Locate and identify every blood parasite.
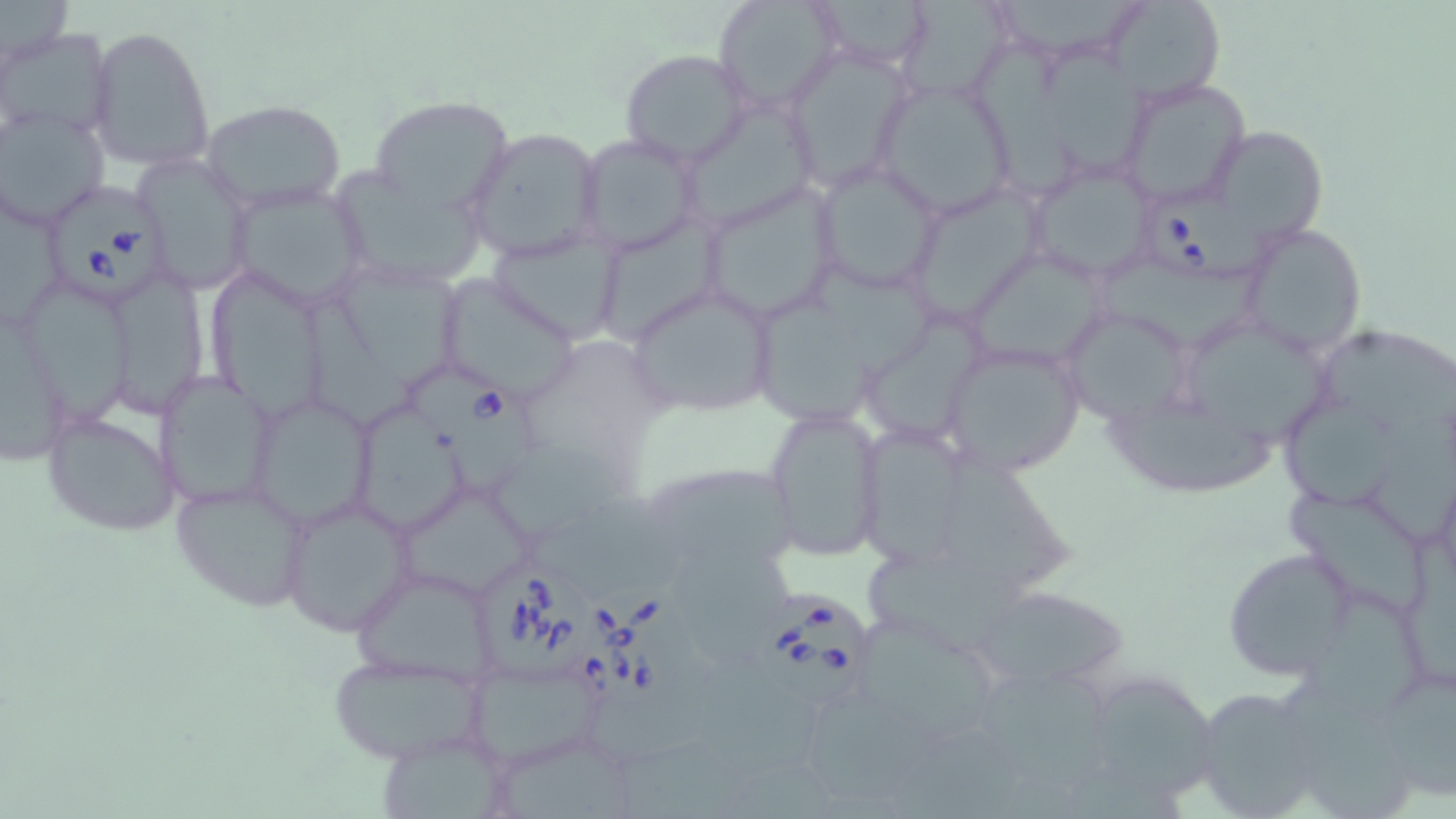

Approximate bounding boxes as (x1,y1)-(x2,y2) corner pairs in pixels.
Babesia divergens-infected red blood cells: (49,186)-(164,306), (1144,189)-(1271,283), (405,367)-(540,498), (477,565)-(592,681), (576,577)-(698,712), (750,590)-(873,713).
No Plasmodium falciparum, Plasmodium ovale, Plasmodium malariae, Plasmodium vivax, or Trypanosoma brucei observed.

slide-level diagnosis = Babesia divergens
preparation = thin blood smear
field of view = one of a larger specimen
magnification = 1000x
stain = May-Grünwald-Giemsa
modality = light microscopy
uninfected red blood cell locations = approximate bounding boxes as (x1,y1)-(x2,y2) corner pairs in pixels: (0,0)-(72,63), (714,0)-(841,115), (803,0)-(935,72), (998,0)-(1151,53), (1109,0)-(1223,105), (896,1)-(1016,104), (86,24)-(216,172), (0,29)-(118,146), (978,33)-(1081,195), (780,44)-(916,193), (1048,49)-(1156,180), (619,50)-(752,166), (1116,76)-(1252,210), (877,80)-(1016,217), (369,96)-(514,215), (202,99)-(346,212), (682,100)-(819,226), (1,107)-(109,230), (1217,127)-(1330,244), (463,128)-(605,263), (577,134)-(704,258), (131,150)-(254,295), (1023,158)-(1160,286), (814,160)-(946,294), (333,171)-(487,290), (916,180)-(1056,326), (2,181)-(68,332), (225,181)-(372,310), (697,182)-(844,324), (602,215)-(727,353), (1236,223)-(1367,356), (484,228)-(628,345), (964,249)-(1112,366), (1095,257)-(1268,358), (807,260)-(932,376), (339,266)-(457,389), (214,269)-(330,426), (110,271)-(203,417), (439,271)-(580,400), (26,280)-(133,427), (624,281)-(780,419), (759,292)-(888,429), (302,293)-(422,428), (1061,302)-(1198,424), (1,309)-(73,468), (866,314)-(992,451), (1186,322)-(1329,439), (1319,333)-(1456,431), (938,338)-(1087,477), (155,370)-(278,510), (248,391)-(379,529), (1284,395)-(1402,515), (360,399)-(469,531), (763,402)-(886,562), (41,404)-(183,538), (1110,410)-(1281,504), (1366,416)-(1456,547), (858,426)-(971,566), (492,446)-(627,536), (945,451)-(1076,605), (653,467)-(803,570), (170,478)-(313,613), (1283,487)-(1429,611), (402,489)-(538,594), (277,494)-(419,636), (529,495)-(694,590), (1403,534)-(1456,683), (679,537)-(787,659), (1223,547)-(1355,678), (865,558)-(1036,653), (352,565)-(500,686), (983,591)-(1132,682), (1303,591)-(1430,714), (852,610)-(1008,749), (460,652)-(606,768), (326,653)-(488,764), (705,659)-(833,773), (980,661)-(1119,793), (1372,665)-(1456,796), (1288,672)-(1414,819), (1095,686)-(1223,794), (1192,686)-(1327,817), (802,699)-(949,799), (498,736)-(638,819), (617,737)-(750,819), (385,743)-(510,819)
image size = 1456×819 pixels